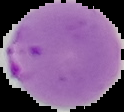 Malaria status: parasitized. Segmented cell region on a black background. Image is 124×112 pixels. From a thin blood film.